Comment on the morphology of the erythrocytes.
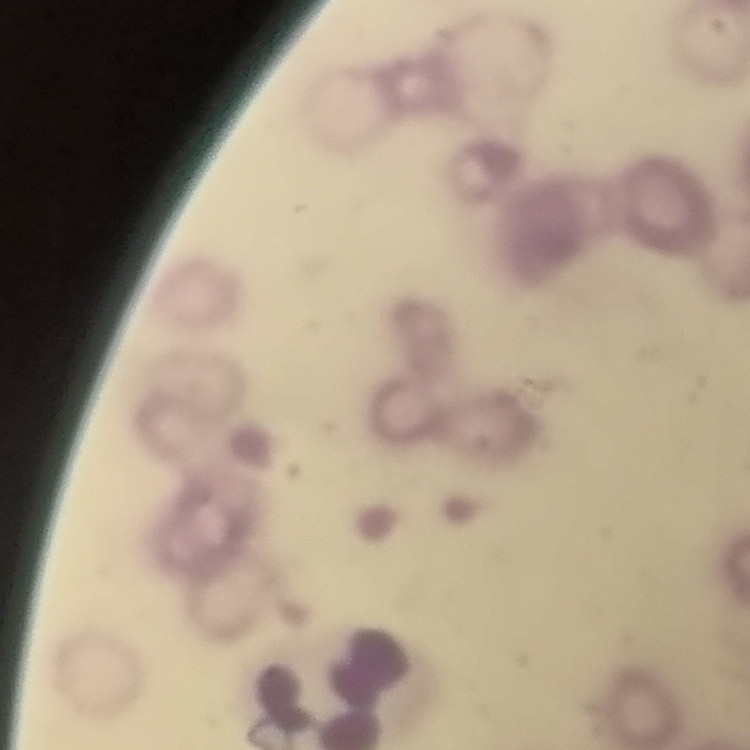

They show rouleaux formation.

Thin blood film. Stained with either Field's or Giemsa. Square crop of a larger photomicrograph.